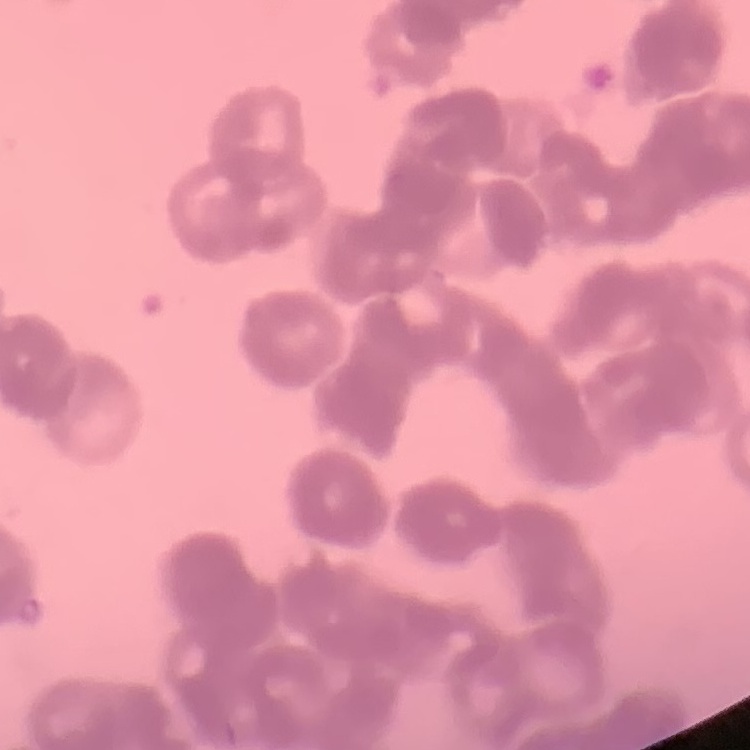 The red blood cells exhibit rouleaux formation. Stained with either Field's or Giemsa. Thin peripheral smear. Square crop of a larger photomicrograph.